Describe the morphology of the red blood cells.
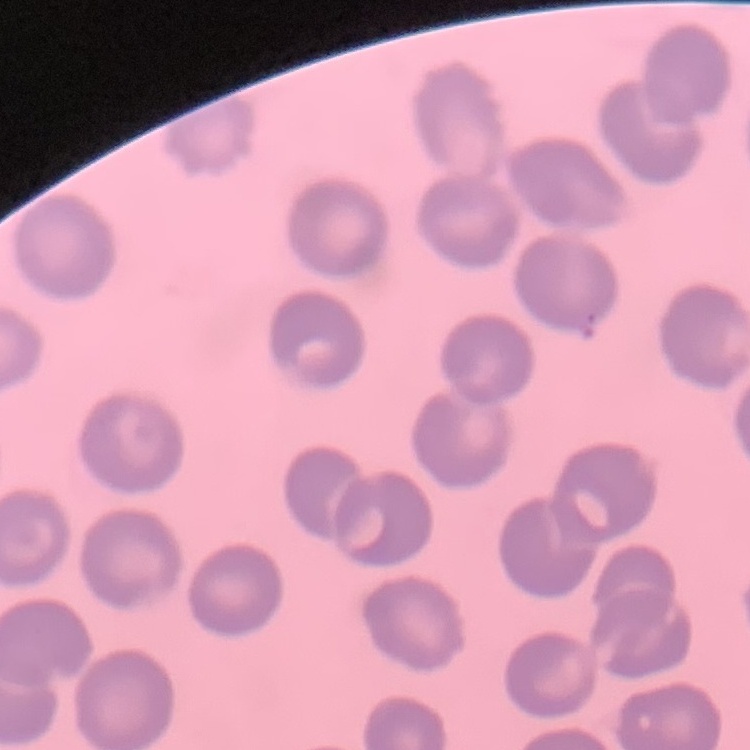
No rouleaux formation.

{
  "preparation": "thin blood film",
  "image_type": "square crop of a larger photomicrograph",
  "stain": "Field's or Giemsa"
}